Assess the morphology of the red blood cells.
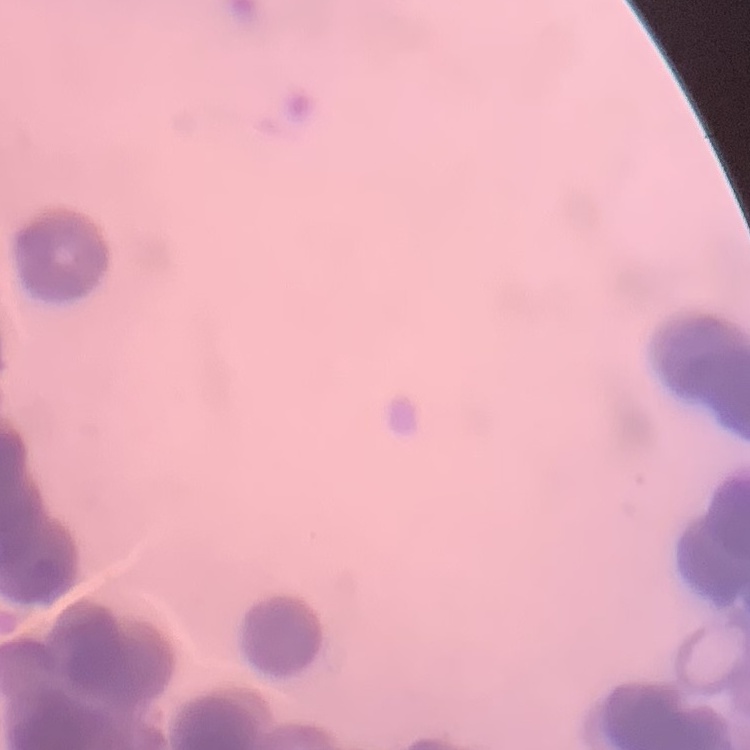

Rouleaux formation.

image type = square crop of a larger photomicrograph
preparation = thin blood film
stain = Field's or Giemsa